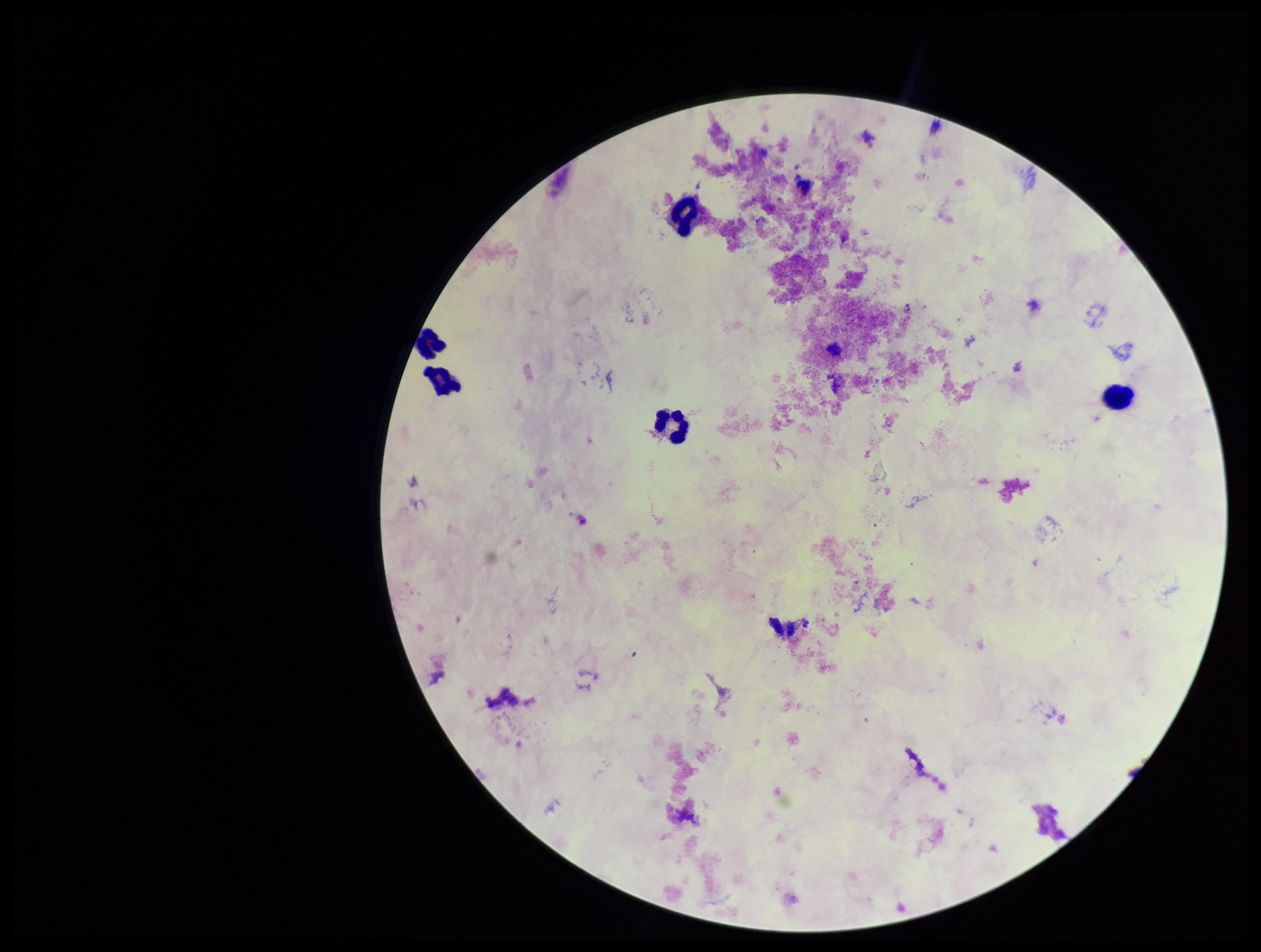
Summary:
  - Leukocyte count: 5
  - Preparation: thick blood smear
  - Image size: 1261×952 pixels
  - Field of view: one from this slide
  - Capture: smartphone photograph through the microscope eyepiece
  - Plasmodium parasites: none detected
  - Parasite count: 0
  - Stain: Giemsa
  - Patient malaria status: negative